Identify the blood parasite species.
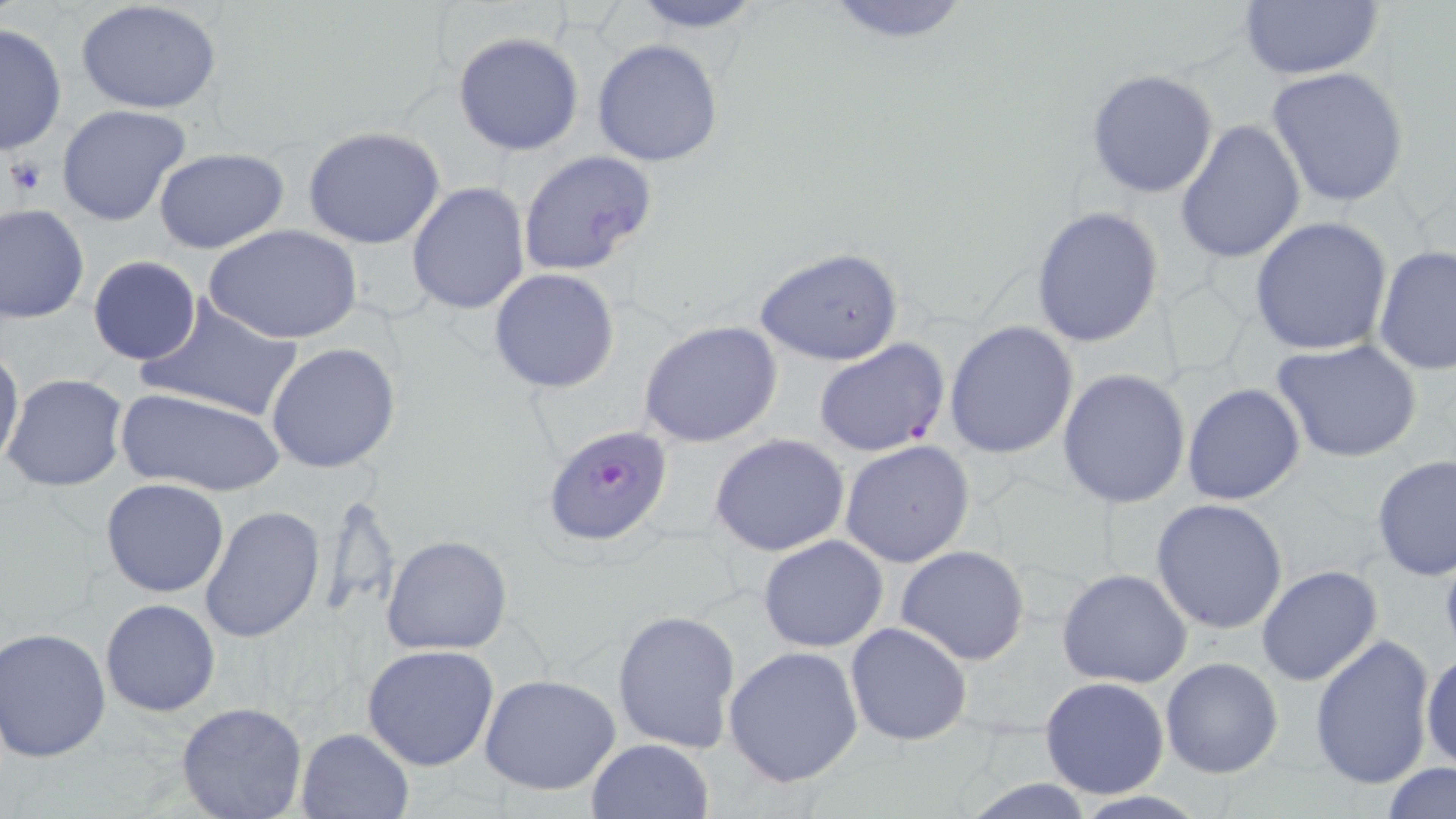
Plasmodium falciparum.

Approximate bounding boxes as (x1, y1, x2, y2) in pixels. Platelet locations: (3, 154, 48, 199). Plasmodium falciparum-infected red blood cell locations: (813, 340, 950, 458), (542, 423, 675, 546). Uninfected red blood cell locations: (623, 0, 770, 35), (818, 0, 976, 47), (1236, 0, 1388, 80), (76, 1, 224, 115), (0, 22, 66, 157), (453, 32, 584, 156), (592, 40, 724, 167), (1266, 65, 1409, 207), (1085, 69, 1218, 198), (56, 104, 193, 227), (1174, 119, 1305, 265), (302, 126, 448, 249), (152, 147, 291, 255), (515, 150, 661, 279), (406, 182, 530, 317), (1, 203, 90, 323), (1031, 205, 1164, 348), (1249, 218, 1394, 357), (206, 224, 363, 347), (1373, 244, 1455, 379), (755, 245, 905, 367), (87, 256, 201, 366), (488, 269, 620, 394), (138, 296, 306, 422), (638, 319, 784, 449), (944, 320, 1079, 459), (1272, 338, 1426, 464), (265, 342, 402, 474), (0, 344, 25, 472), (1057, 368, 1190, 509), (4, 373, 129, 492), (1181, 382, 1306, 506), (114, 386, 283, 495), (710, 434, 850, 556), (840, 440, 976, 569), (1372, 454, 1455, 581), (101, 477, 230, 598), (316, 487, 401, 623), (1151, 499, 1289, 634), (199, 504, 326, 644), (381, 534, 513, 656), (757, 534, 888, 653), (896, 545, 1031, 666), (1256, 563, 1384, 686), (1056, 567, 1193, 688), (101, 599, 219, 716), (611, 608, 742, 754), (845, 622, 971, 747), (1, 628, 115, 763), (1308, 634, 1437, 790), (362, 644, 499, 771), (723, 644, 864, 786), (1421, 649, 1456, 770), (1160, 656, 1284, 780), (479, 673, 622, 796), (1039, 676, 1170, 800), (174, 701, 308, 819), (295, 727, 414, 818), (587, 738, 714, 818), (1381, 761, 1455, 817), (960, 779, 1101, 817), (1064, 791, 1212, 819). 1000x magnification. Optical microscopy. One field of a larger specimen. Thin blood smear. May-Grünwald-Giemsa stain. Image is 1456×819 pixels.